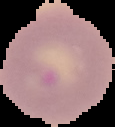
Summary:
  - Image size: 115×127 pixels
  - Result: Plasmodium parasites detected
  - Image type: segmented cell region with the area outside set to black
  - Preparation: thin blood smear